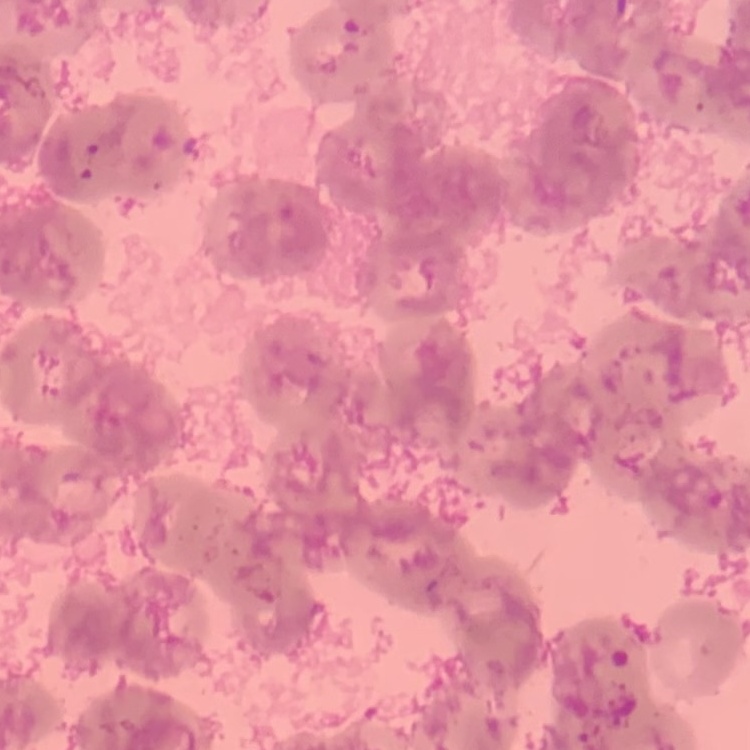
Summary:
  - Red blood cell morphology: rouleaux formation
  - Preparation: thin blood smear
  - Image type: square crop of a larger photomicrograph
  - Stain: Field's or Giemsa